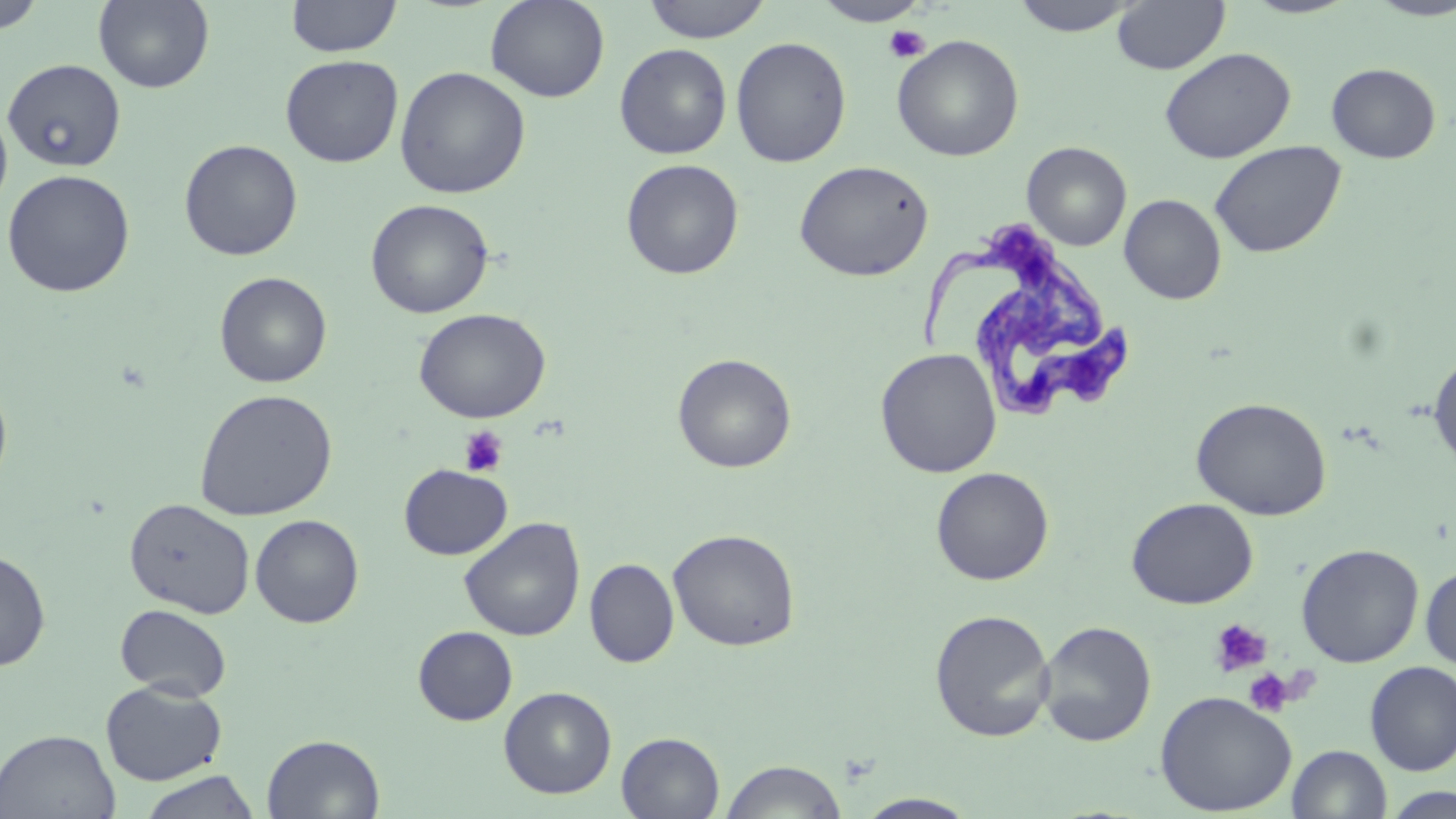

Summary:
  - Coordinate format: approximate bounding boxes as (x1, y1, x2, y2) in pixels
  - Uninfected red blood cell locations: (0, 0, 46, 34), (94, 0, 215, 93), (285, 0, 402, 58), (485, 0, 610, 103), (639, 0, 773, 43), (1008, 0, 1145, 37), (1112, 0, 1230, 76), (1367, 0, 1456, 21), (811, 1, 933, 27), (892, 35, 1024, 162), (730, 36, 852, 168), (614, 43, 732, 159), (1159, 47, 1296, 164), (280, 54, 403, 167), (2, 59, 126, 171), (1326, 62, 1442, 164), (394, 66, 531, 199), (0, 104, 13, 218), (179, 139, 303, 261), (1209, 140, 1347, 259), (1022, 142, 1132, 251), (620, 158, 744, 280), (794, 160, 934, 282), (1, 169, 136, 297), (1119, 193, 1226, 305), (365, 198, 494, 319), (214, 271, 332, 388), (414, 307, 551, 423), (875, 347, 1002, 477), (1428, 349, 1456, 475), (672, 353, 797, 473), (0, 377, 13, 498), (194, 388, 337, 521), (1191, 396, 1332, 521), (399, 464, 513, 560), (931, 466, 1054, 586), (124, 497, 255, 618), (1127, 497, 1258, 609), (250, 514, 364, 628), (459, 517, 585, 641), (668, 528, 801, 651), (1296, 543, 1424, 668), (0, 548, 51, 672), (584, 558, 679, 667), (1420, 563, 1456, 671), (115, 603, 232, 701), (928, 608, 1056, 742), (1037, 620, 1157, 747), (413, 626, 517, 725), (1364, 662, 1456, 776), (100, 680, 227, 786), (499, 686, 617, 798), (1155, 690, 1297, 816), (1, 728, 121, 818), (617, 732, 725, 818), (261, 733, 385, 818), (1288, 745, 1391, 819), (719, 758, 848, 819), (136, 770, 261, 819), (1382, 786, 1456, 819), (855, 793, 980, 818)
  - Platelet locations: (883, 24, 930, 63), (458, 425, 509, 477), (1209, 618, 1272, 677), (1243, 668, 1293, 717)
  - Trypanosoma brucei locations: (920, 219, 1135, 435)
  - Slide-level diagnosis: Trypanosoma brucei
  - Field of view: single
  - Modality: light microscopy
  - Stain: May-Grünwald-Giemsa
  - Magnification: 1000x
  - Image size: 1456×819 pixels
  - Preparation: thin blood film